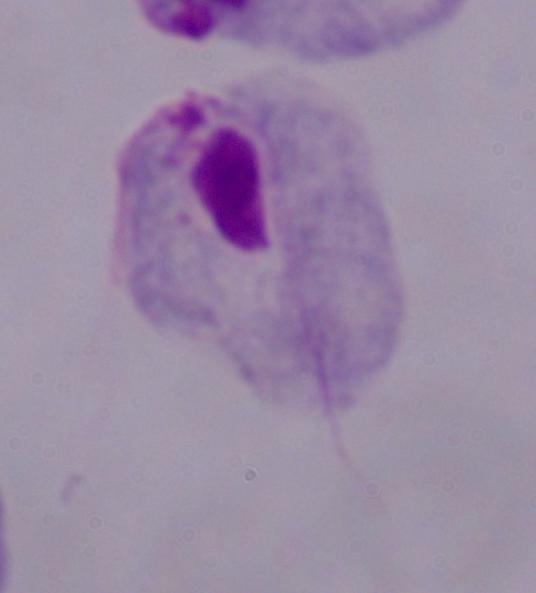

modality = micrograph
magnification = 1000x
identification = trichomonad